Identify the parasite.
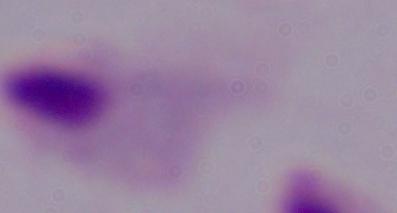
A trichomonad.

Photomicrograph. 1000x magnification.